Classify this cell by malaria status.
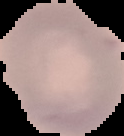

Uninfected.

image type = cell region segmented out of the field of view; surrounding area masked to black
preparation = thin blood smear
image size = 124×136 pixels